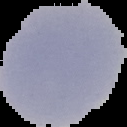
From a thin blood smear. Image is 127×127 pixels. Result: negative for Plasmodium parasites. The area outside the segmented cell region is set to black.